Name the blood parasite species.
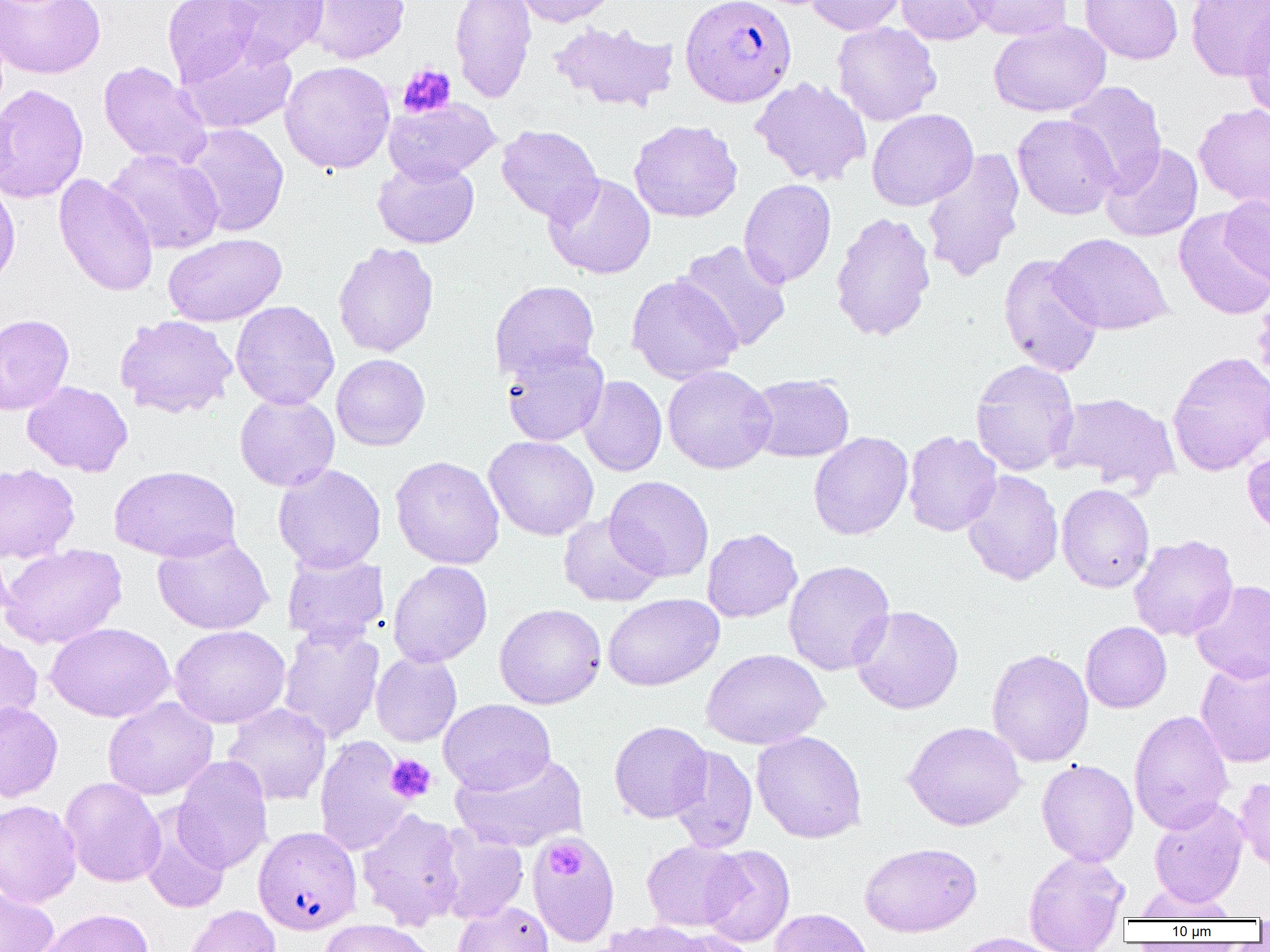

Plasmodium falciparum.

{
  "platelet_locations": "approximate bounding boxes as (x1, y1, x2, y2) in pixels: (397, 63, 456, 118), (386, 754, 437, 803), (546, 841, 584, 878)",
  "preparation": "thin blood smear",
  "plasmodium_falciparum_infected_red_blood_cell_locations": "approximate bounding boxes as (x1, y1, x2, y2) in pixels: (680, 0, 797, 107), (253, 826, 363, 935)",
  "magnification": "1000x",
  "modality": "light microscopy",
  "image_size": "1270×952 pixels",
  "uninfected_red_blood_cell_locations": "approximate bounding boxes as (x1, y1, x2, y2) in pixels: (0, 0, 106, 80), (162, 0, 262, 86), (221, 0, 331, 67), (305, 0, 410, 64), (450, 0, 537, 103), (513, 0, 620, 27), (806, 0, 906, 36), (894, 0, 995, 45), (963, 0, 1072, 41), (1080, 0, 1183, 65), (1186, 0, 1270, 81), (1240, 9, 1270, 121), (549, 20, 679, 113), (989, 21, 1111, 117), (831, 22, 941, 126), (180, 40, 297, 135), (279, 60, 395, 174), (98, 61, 213, 169), (750, 76, 872, 186), (1064, 81, 1167, 195), (0, 84, 89, 204), (384, 97, 501, 184), (1194, 103, 1270, 209), (866, 108, 978, 211), (1012, 114, 1120, 220), (628, 119, 742, 223), (180, 123, 290, 237), (496, 125, 603, 223), (1101, 143, 1203, 242), (104, 149, 225, 255), (921, 150, 1025, 283), (372, 159, 480, 249), (53, 173, 159, 298), (544, 173, 656, 279), (0, 177, 20, 291), (738, 179, 837, 288), (1220, 191, 1270, 288), (1174, 208, 1270, 320), (830, 211, 936, 342), (163, 233, 286, 327), (1050, 233, 1172, 335), (675, 240, 792, 353), (333, 242, 439, 358), (998, 253, 1103, 378), (626, 274, 742, 384), (490, 280, 600, 382), (231, 300, 339, 410), (0, 314, 74, 415), (114, 314, 238, 418), (501, 343, 609, 446), (1166, 350, 1270, 477), (330, 353, 430, 451), (970, 359, 1079, 476), (662, 365, 776, 474), (747, 374, 854, 462), (578, 375, 667, 477), (22, 381, 133, 477), (1052, 391, 1181, 495), (234, 394, 340, 492), (902, 430, 1002, 536), (808, 431, 913, 540), (484, 435, 599, 541), (1243, 446, 1270, 539), (390, 455, 505, 569), (0, 463, 80, 564), (109, 464, 241, 562), (273, 464, 386, 574), (962, 470, 1064, 585), (605, 475, 714, 582), (1056, 483, 1155, 593), (558, 513, 664, 607), (702, 528, 803, 622), (152, 534, 273, 635), (1129, 534, 1238, 642), (0, 538, 13, 628), (0, 543, 126, 649), (282, 552, 388, 646), (783, 560, 895, 675), (387, 561, 493, 667), (1191, 579, 1270, 683), (603, 593, 724, 691), (494, 603, 606, 709), (850, 605, 963, 715), (1081, 621, 1172, 713), (45, 622, 175, 723), (169, 624, 290, 728), (279, 625, 384, 743), (0, 633, 44, 734), (701, 648, 828, 750), (987, 648, 1094, 767), (370, 650, 462, 747), (1195, 659, 1270, 768), (103, 697, 218, 800), (438, 698, 556, 794), (0, 701, 63, 803), (222, 703, 331, 806), (1129, 710, 1234, 834), (609, 721, 713, 823), (903, 721, 1026, 831), (751, 730, 867, 844), (315, 736, 413, 856), (668, 745, 758, 853), (451, 752, 587, 853), (173, 756, 273, 874), (1036, 759, 1139, 867), (1234, 776, 1270, 875), (59, 777, 167, 887), (0, 799, 82, 907), (1149, 800, 1249, 907), (140, 804, 230, 914), (357, 808, 466, 930), (435, 825, 529, 924), (527, 834, 620, 945), (642, 840, 746, 931), (860, 842, 981, 937), (700, 845, 795, 947), (1023, 850, 1129, 951), (1132, 882, 1238, 921), (0, 885, 59, 952), (452, 901, 553, 952), (182, 904, 282, 952), (35, 907, 154, 952), (769, 908, 874, 952), (318, 918, 437, 952), (600, 920, 717, 952), (659, 928, 761, 952), (948, 933, 1068, 952)",
  "field_of_view": "one of a larger specimen"
}